Assess this cell for malaria.
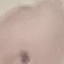
Uninfected.

Acquired by smartphone through the microscope eyepiece. Thin blood film. Giemsa stain. Cell patch, automatically extracted from a larger field of view and resized to 64 × 64 pixels.